State which parasite is depicted.
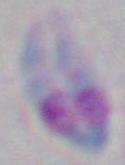
This is Toxoplasma gondii.

modality: micrograph
magnification: 1000x